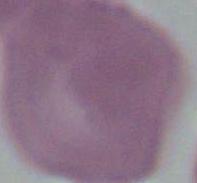 Captured at 1000x magnification. An erythrocyte is seen. Micrograph.